Give the extent of all uninfected red blood cells.
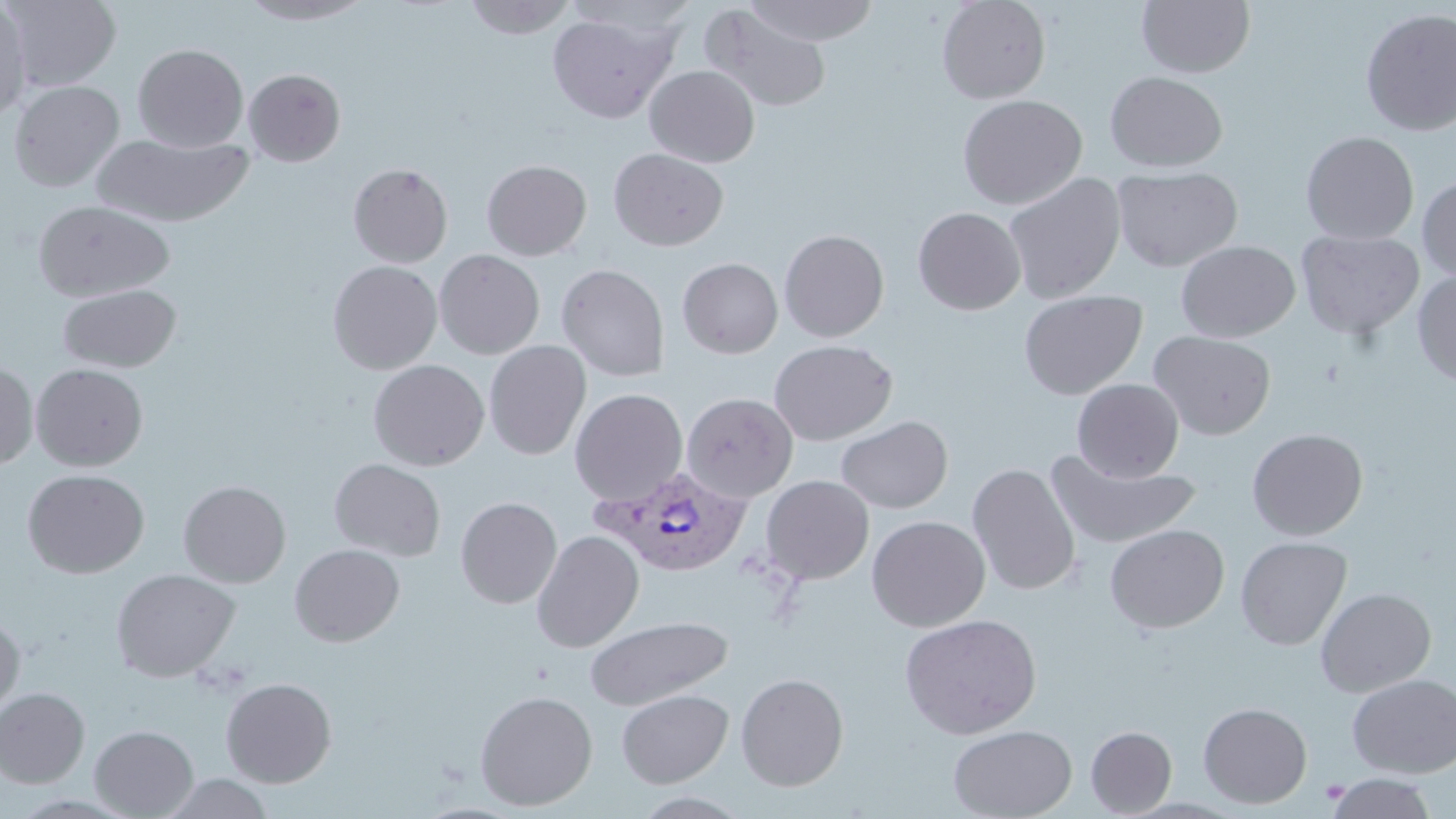

Approximate bounding boxes as [x1, y1, x2, y2] in pixels.
Uninfected red blood cells: [2, 0, 121, 91], [238, 0, 377, 25], [463, 0, 579, 40], [936, 0, 1051, 104], [744, 1, 881, 46], [1137, 1, 1255, 77], [0, 2, 32, 123], [700, 4, 832, 114], [1360, 7, 1456, 137], [547, 10, 678, 123], [132, 43, 248, 153], [645, 65, 760, 167], [243, 68, 346, 166], [1105, 71, 1228, 172], [8, 79, 125, 191], [957, 94, 1087, 209], [1300, 131, 1420, 245], [91, 132, 254, 227], [609, 148, 729, 251], [482, 159, 591, 260], [348, 163, 453, 267], [1111, 166, 1243, 272], [1002, 172, 1126, 304], [1417, 175, 1456, 282], [32, 200, 175, 302], [913, 206, 1026, 315], [778, 229, 890, 342], [1296, 229, 1425, 340], [1175, 240, 1300, 343], [434, 250, 545, 359], [433, 257, 671, 372], [677, 257, 783, 358], [328, 260, 442, 374], [556, 263, 670, 381], [1412, 270, 1456, 385], [57, 283, 182, 373], [1018, 289, 1148, 400], [1149, 330, 1276, 439], [769, 339, 897, 445], [484, 340, 591, 460], [368, 359, 490, 471], [0, 363, 38, 470], [31, 363, 148, 471], [1071, 379, 1184, 482], [570, 388, 688, 505], [681, 392, 798, 502], [836, 415, 953, 514], [1247, 428, 1368, 540], [1047, 453, 1202, 550], [329, 458, 445, 561], [967, 463, 1081, 596], [22, 469, 150, 578], [760, 475, 874, 585], [178, 480, 291, 587], [455, 497, 562, 608], [866, 515, 990, 632], [1105, 524, 1230, 634], [531, 530, 644, 652], [1235, 536, 1352, 650], [289, 544, 405, 647], [110, 568, 240, 682], [1315, 588, 1436, 697], [899, 613, 1042, 740], [585, 615, 733, 710], [0, 616, 25, 717], [736, 672, 849, 791], [1346, 674, 1456, 777], [220, 677, 337, 787], [0, 688, 90, 788], [616, 688, 734, 787], [474, 689, 598, 811], [1198, 702, 1313, 809], [948, 724, 1077, 819], [90, 725, 198, 818], [1086, 726, 1177, 817], [1325, 773, 1438, 819], [160, 774, 275, 819].

Platelet locations: [1320, 778, 1349, 804]. Plasmodium vivax-infected red blood cell locations: [593, 466, 751, 577]. Slide-level diagnosis: Plasmodium vivax. Thin blood film. May-Grünwald-Giemsa-stained preparation. Image is 1456×819 pixels. Optical microscopy. Captured at 1000x magnification. One field of a larger specimen.